Classify this cell by malaria status.
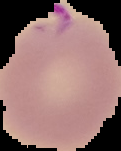
It is parasitized.

preparation: thin blood smear
image_type: cell region segmented out of the field of view; surrounding area masked to black
image_size: 121×151 pixels